Outline each Plasmodium ovale-infected red blood cell.
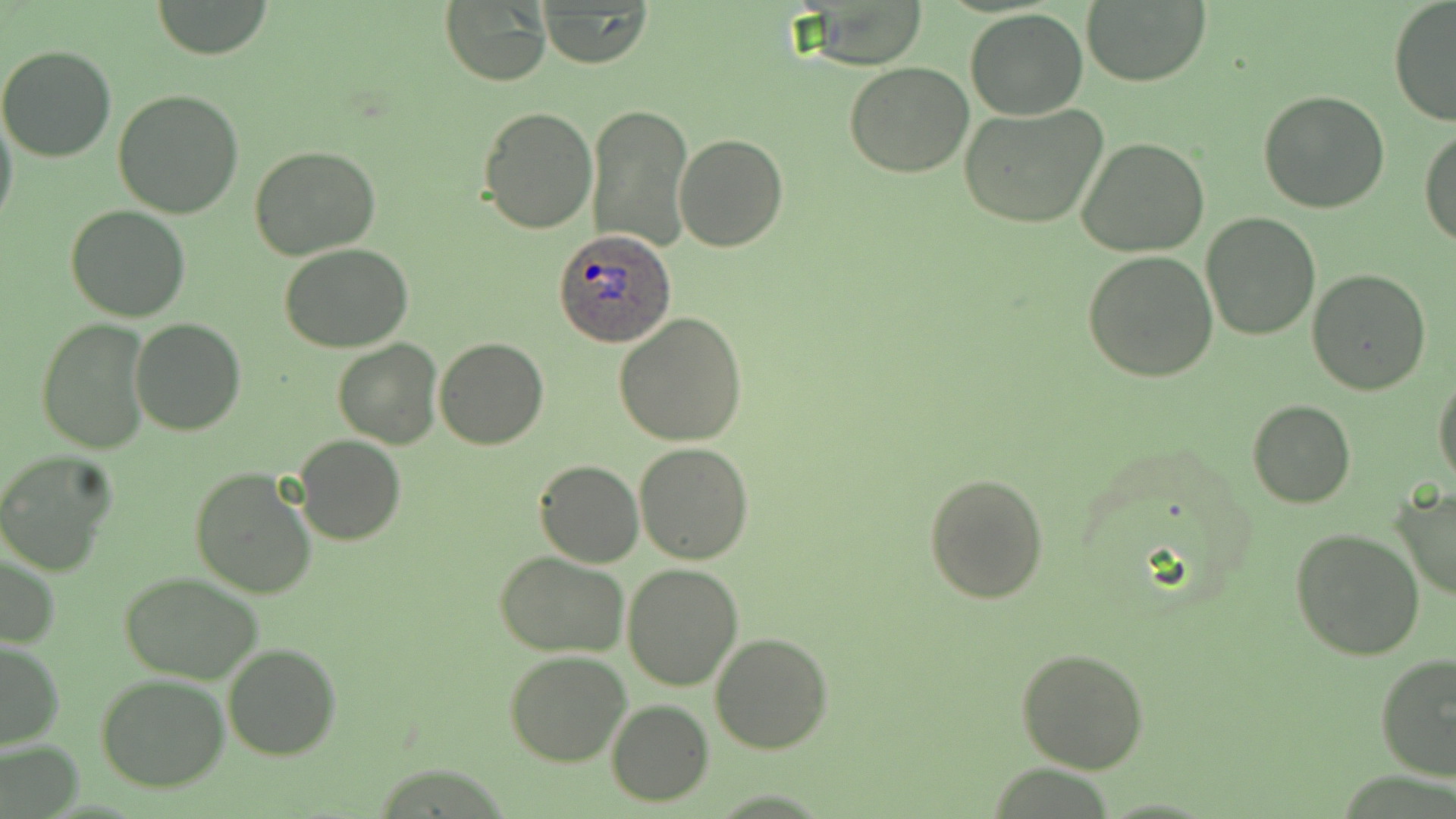
Approximate bounding boxes as [x1, y1, x2, y2] in pixels.
Plasmodium ovale-infected red blood cells: [555, 229, 676, 348].

Uninfected red blood cell locations: [147, 1, 273, 59], [1081, 1, 1211, 86], [1387, 1, 1456, 127], [438, 2, 551, 86], [537, 3, 652, 68], [965, 10, 1088, 119], [0, 45, 117, 163], [844, 61, 975, 177], [112, 89, 244, 219], [1258, 90, 1390, 212], [586, 102, 692, 252], [478, 103, 599, 234], [958, 103, 1109, 229], [0, 106, 17, 234], [1419, 125, 1456, 247], [674, 133, 788, 253], [1075, 136, 1209, 257], [248, 145, 382, 260], [64, 204, 191, 322], [1201, 212, 1322, 340], [277, 243, 413, 352], [1082, 251, 1219, 382], [1307, 268, 1433, 395], [614, 312, 747, 447], [37, 319, 151, 453], [130, 320, 245, 437], [435, 337, 548, 450], [332, 339, 444, 450], [1433, 369, 1456, 488], [1246, 399, 1357, 508], [293, 436, 405, 545], [633, 442, 753, 564], [0, 452, 116, 576], [535, 460, 644, 568], [189, 468, 317, 599], [923, 471, 1049, 604], [1390, 485, 1456, 602], [1291, 527, 1426, 663], [496, 551, 627, 657], [0, 552, 59, 651], [623, 561, 744, 691], [118, 570, 267, 683], [710, 632, 833, 753], [0, 640, 65, 748], [223, 643, 341, 762], [1017, 646, 1149, 774], [505, 650, 632, 767], [1376, 652, 1456, 782], [97, 674, 230, 791], [607, 699, 713, 805], [1, 741, 83, 817]. Slide-level diagnosis: Plasmodium ovale. Captured at 1000x magnification. One field of a larger specimen. Thin blood smear. Image is 1456×819 pixels. May-Grünwald-Giemsa stain. Light microscopy.